Name the cell type shown.
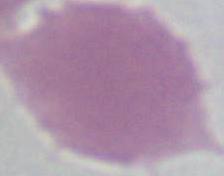

This is an erythrocyte.

modality = photomicrograph
magnification = 1000x